Give the extent of all uninfected red blood cells.
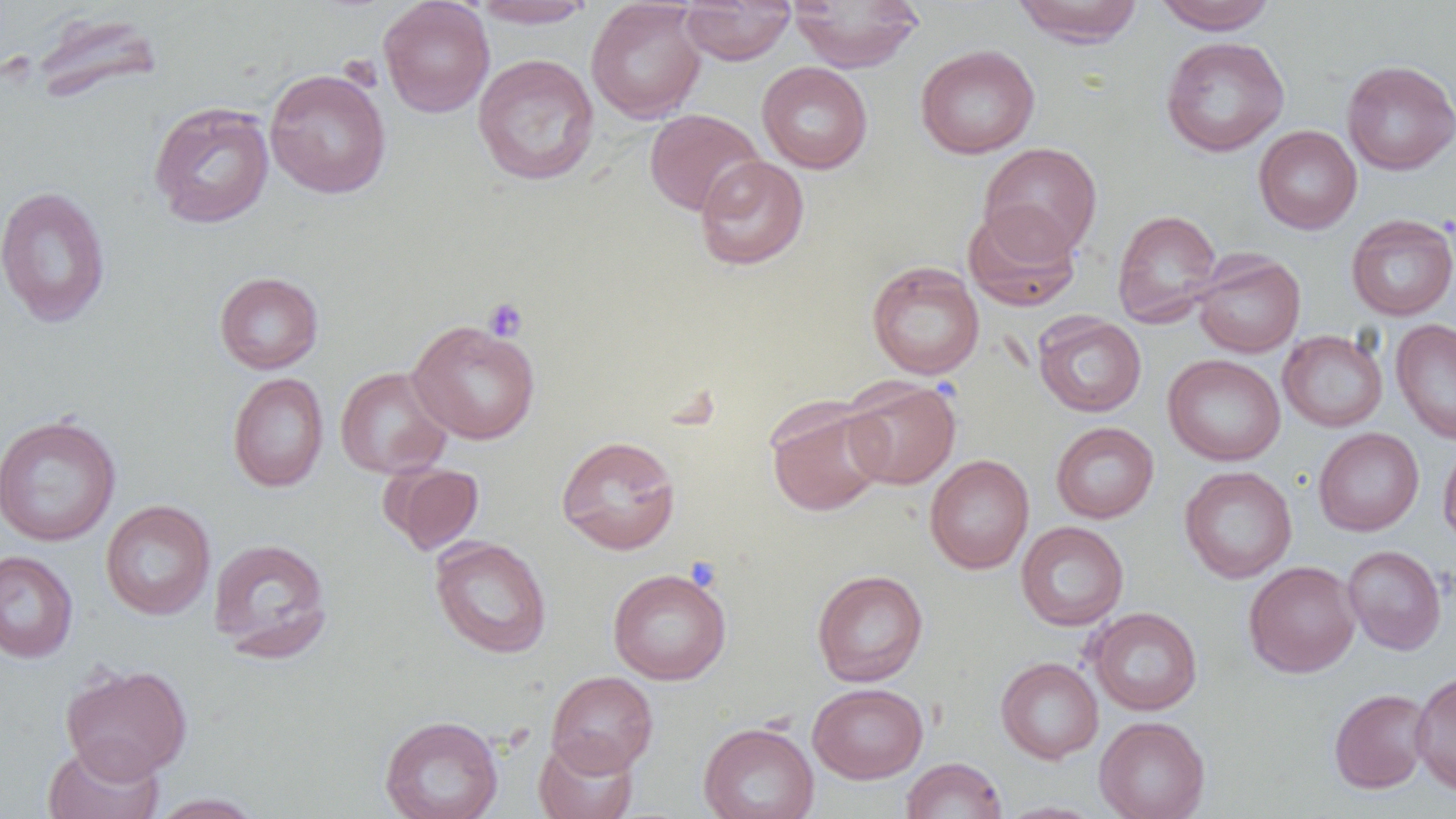

Approximate bounding boxes as [x1, y1, x2, y2] in pixels.
Uninfected red blood cells: [378, 0, 495, 118], [470, 0, 596, 29], [788, 0, 924, 72], [1011, 0, 1145, 48], [1152, 0, 1277, 34], [585, 1, 706, 123], [679, 1, 796, 65], [33, 12, 162, 105], [1161, 36, 1290, 157], [915, 44, 1040, 159], [473, 53, 599, 186], [1341, 59, 1456, 175], [757, 61, 873, 174], [265, 68, 392, 200], [148, 101, 274, 229], [644, 109, 766, 217], [1253, 125, 1362, 234], [978, 142, 1102, 259], [694, 155, 809, 271], [0, 186, 111, 328], [963, 204, 1081, 312], [1112, 209, 1223, 327], [1345, 214, 1456, 321], [1192, 250, 1305, 358], [866, 261, 984, 380], [214, 272, 324, 374], [1033, 313, 1147, 417], [1390, 318, 1456, 444], [408, 319, 541, 444], [1278, 329, 1388, 432], [1162, 354, 1285, 466], [335, 366, 452, 479], [227, 372, 329, 492], [842, 376, 961, 490], [766, 399, 889, 517], [0, 414, 121, 547], [1050, 421, 1159, 523], [1313, 427, 1424, 536], [556, 434, 682, 555], [1438, 438, 1456, 551], [924, 454, 1034, 574], [380, 462, 484, 555], [1179, 465, 1297, 584], [100, 500, 215, 620], [1015, 521, 1129, 631], [430, 536, 552, 658], [207, 537, 332, 662], [1342, 545, 1447, 655], [0, 550, 78, 663], [1243, 560, 1360, 678], [607, 568, 731, 685], [812, 569, 928, 687], [1087, 607, 1203, 715], [995, 657, 1103, 763], [60, 662, 193, 781], [546, 670, 658, 776], [1410, 670, 1456, 795], [808, 682, 928, 783], [1329, 688, 1432, 793], [379, 714, 504, 819], [1094, 716, 1210, 819], [698, 721, 819, 819], [534, 735, 638, 819], [42, 738, 164, 819], [901, 757, 1007, 818], [147, 792, 266, 818], [995, 801, 1107, 819].

Platelet locations: [482, 297, 528, 342], [685, 557, 723, 593]. Slide-level diagnosis: negative for blood parasites. Image is 1456×819 pixels. 1000x magnification. One field of a larger specimen. Thin blood smear. Optical microscopy.